Report the malaria status of this cell.
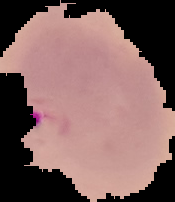
It is parasitized.

Summary:
  - Preparation: thin blood film
  - Image size: 175×202 pixels
  - Image type: segmented cell region with the area outside set to black